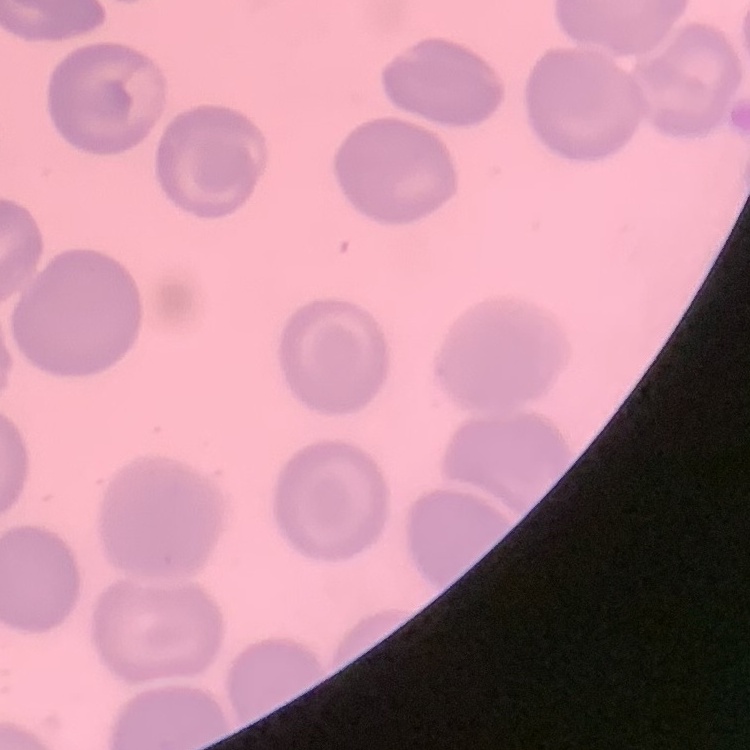
red blood cell morphology = no rouleaux formation
image type = one tile cut from a larger photomicrograph
stain = Field's or Giemsa
preparation = thin blood smear